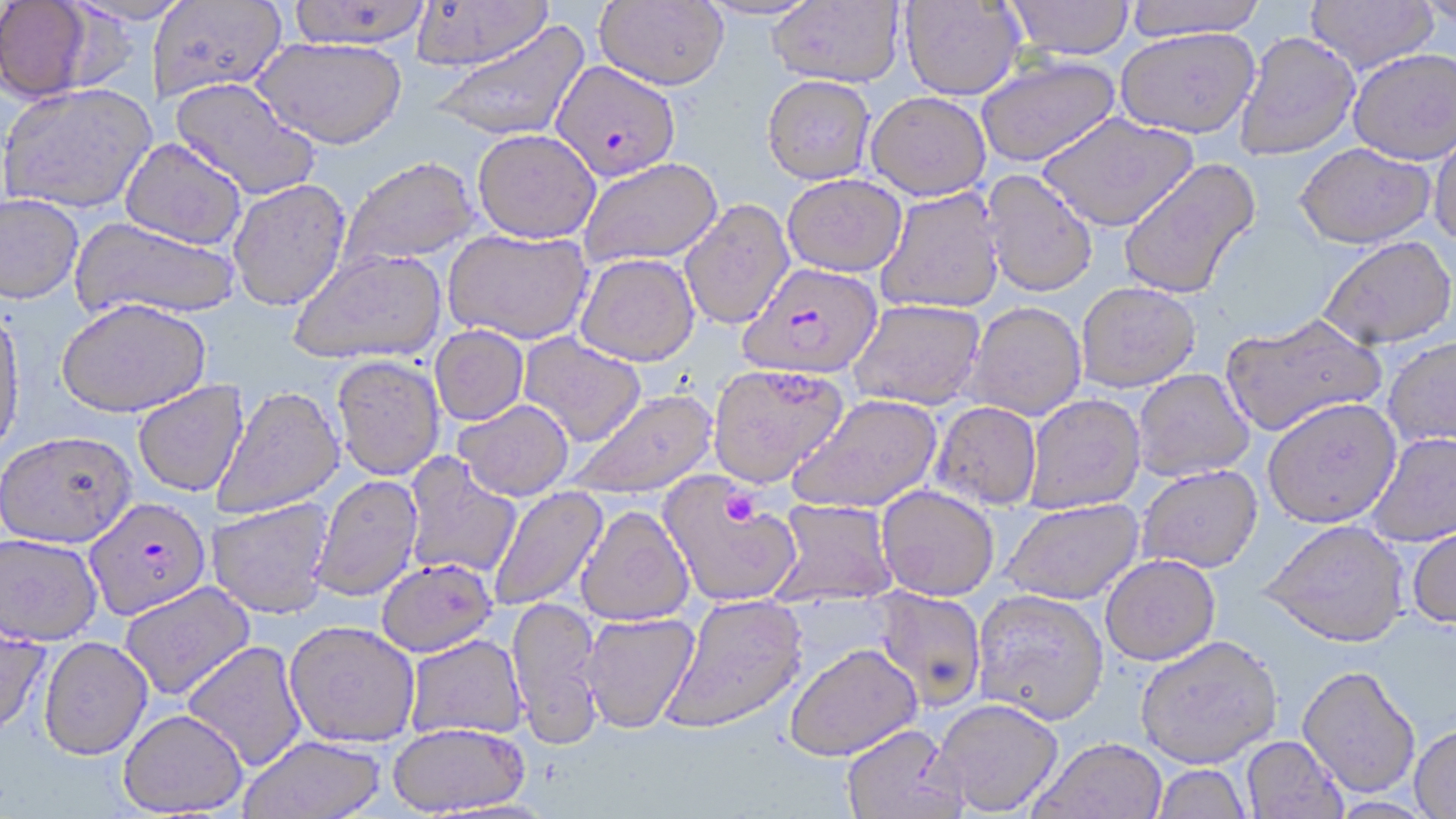 Approximate bounding boxes as [x1, y1, x2, y2] in pixels. Platelet locations: [721, 490, 759, 526]. Plasmodium falciparum-infected red blood cell locations: [550, 61, 681, 182], [740, 263, 883, 379], [86, 498, 211, 621]. Uninfected red blood cell locations: [0, 0, 94, 101], [66, 0, 193, 28], [287, 0, 432, 50], [410, 0, 553, 72], [698, 0, 823, 22], [767, 0, 905, 86], [1122, 0, 1266, 38], [1305, 0, 1439, 74], [1415, 0, 1456, 27], [147, 1, 286, 101], [595, 1, 728, 90], [900, 1, 1026, 100], [1006, 1, 1135, 58], [430, 20, 591, 142], [1116, 26, 1259, 138], [1234, 31, 1360, 161], [253, 36, 407, 149], [1348, 48, 1456, 164], [975, 55, 1122, 168], [761, 75, 876, 185], [170, 77, 321, 202], [1, 83, 157, 214], [866, 91, 991, 200], [1037, 112, 1198, 231], [472, 128, 601, 243], [1429, 128, 1456, 248], [120, 137, 247, 251], [1296, 143, 1436, 248], [338, 156, 479, 270], [577, 158, 722, 268], [1118, 158, 1261, 300], [981, 170, 1098, 297], [781, 173, 907, 277], [227, 178, 351, 312], [875, 188, 1006, 314], [0, 194, 84, 305], [680, 199, 795, 330], [71, 218, 240, 322], [443, 228, 593, 344], [1318, 236, 1456, 350], [288, 248, 447, 365], [575, 253, 700, 367], [1075, 281, 1201, 392], [849, 298, 986, 410], [57, 299, 212, 419], [965, 301, 1087, 420], [0, 307, 26, 464], [1219, 313, 1387, 437], [430, 325, 529, 425], [518, 333, 646, 447], [1383, 337, 1456, 449], [331, 355, 445, 480], [706, 363, 849, 487], [1132, 369, 1255, 481], [133, 380, 249, 497], [212, 385, 345, 519], [569, 389, 717, 500], [1023, 393, 1146, 513], [788, 394, 942, 513], [1262, 397, 1401, 528], [453, 399, 574, 501], [932, 401, 1042, 509], [1365, 431, 1456, 546], [0, 433, 136, 550], [403, 455, 521, 579], [1136, 464, 1263, 573], [311, 474, 423, 602], [659, 475, 801, 608], [876, 485, 1000, 599], [487, 486, 608, 612], [207, 498, 334, 619], [770, 498, 899, 606], [1002, 499, 1144, 604], [574, 506, 694, 627], [1259, 519, 1411, 648], [1407, 524, 1456, 630], [0, 534, 103, 648], [1100, 554, 1221, 665], [376, 558, 497, 657], [119, 582, 256, 700], [871, 588, 987, 710], [972, 589, 1109, 725], [661, 593, 809, 734], [506, 597, 605, 747], [579, 611, 700, 733], [0, 620, 51, 742], [284, 621, 420, 748], [406, 634, 528, 740], [1135, 634, 1283, 768], [38, 638, 153, 763], [182, 641, 307, 772], [784, 642, 923, 761], [1297, 666, 1420, 799], [934, 698, 1064, 815], [118, 711, 248, 817], [842, 723, 966, 819], [387, 724, 532, 816], [1409, 725, 1456, 818], [240, 736, 386, 819], [1242, 736, 1348, 819], [1030, 738, 1168, 819], [1150, 764, 1253, 819]. Slide-level diagnosis: Plasmodium falciparum. 1000x magnification. Image is 1456×819 pixels. May-Grünwald-Giemsa stain. Thin blood smear. One field of a larger specimen. Optical microscopy.